Assess this cell for malaria.
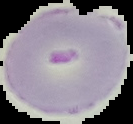
Parasitized.

{
  "preparation": "thin blood film",
  "image_type": "cell region segmented out of the field of view; surrounding area masked to black",
  "image_size": "133×124 pixels"
}